Locate every blood parasite and identify its species.
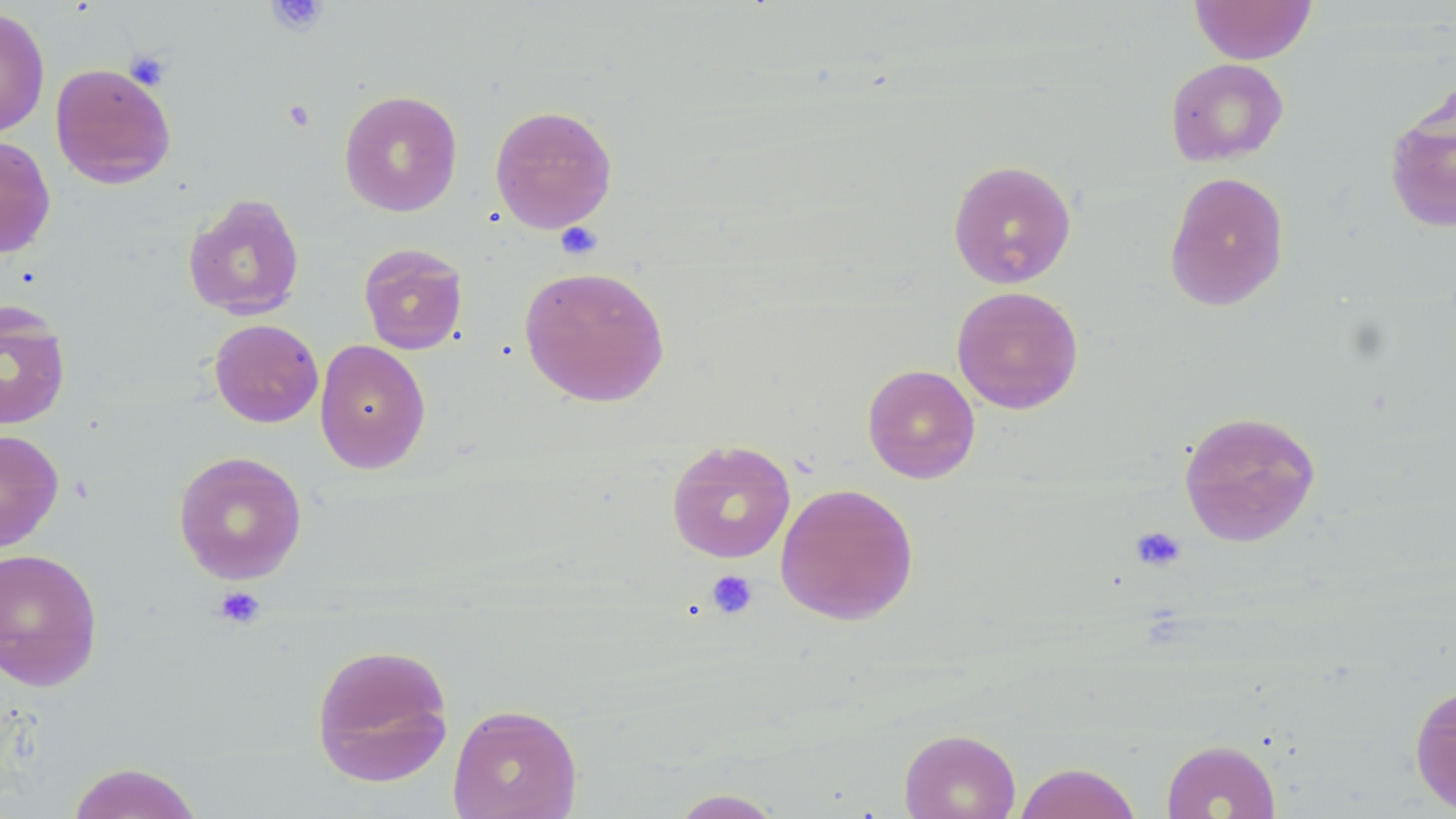
No blood parasites observed.

slide-level diagnosis = no evidence of blood parasites
magnification = 1000x
image size = 1456×819 pixels
platelet locations = approximate bounding boxes as (x1,y1)-(x2,y2) corner pairs in pixels: (268,0)-(329,36), (124,50)-(172,91), (283,100)-(316,131), (555,222)-(603,260), (1131,526)-(1186,572), (706,569)-(758,619), (212,585)-(267,629)
modality = optical microscopy
stain = May-Grünwald-Giemsa
field of view = single
preparation = thin blood film
uninfected red blood cell locations = approximate bounding boxes as (x1,y1)-(x2,y2) corner pairs in pixels: (1189,0)-(1317,64), (0,6)-(50,138), (1165,58)-(1289,166), (50,62)-(176,188), (339,90)-(463,217), (1383,93)-(1456,236), (489,104)-(618,233), (0,135)-(56,258), (947,159)-(1077,290), (1164,171)-(1290,311), (183,193)-(305,321), (358,243)-(468,355), (518,265)-(670,407), (951,285)-(1084,414), (0,304)-(71,431), (209,319)-(323,428), (314,339)-(431,474), (862,364)-(980,484), (1178,410)-(1322,547), (0,429)-(64,551), (666,439)-(796,563), (172,450)-(308,584), (775,483)-(919,625), (0,547)-(103,691), (310,643)-(454,787), (1409,682)-(1456,815), (447,703)-(583,819), (899,728)-(1021,819), (1161,739)-(1281,818), (66,762)-(204,819), (1013,762)-(1143,819), (667,788)-(786,818)